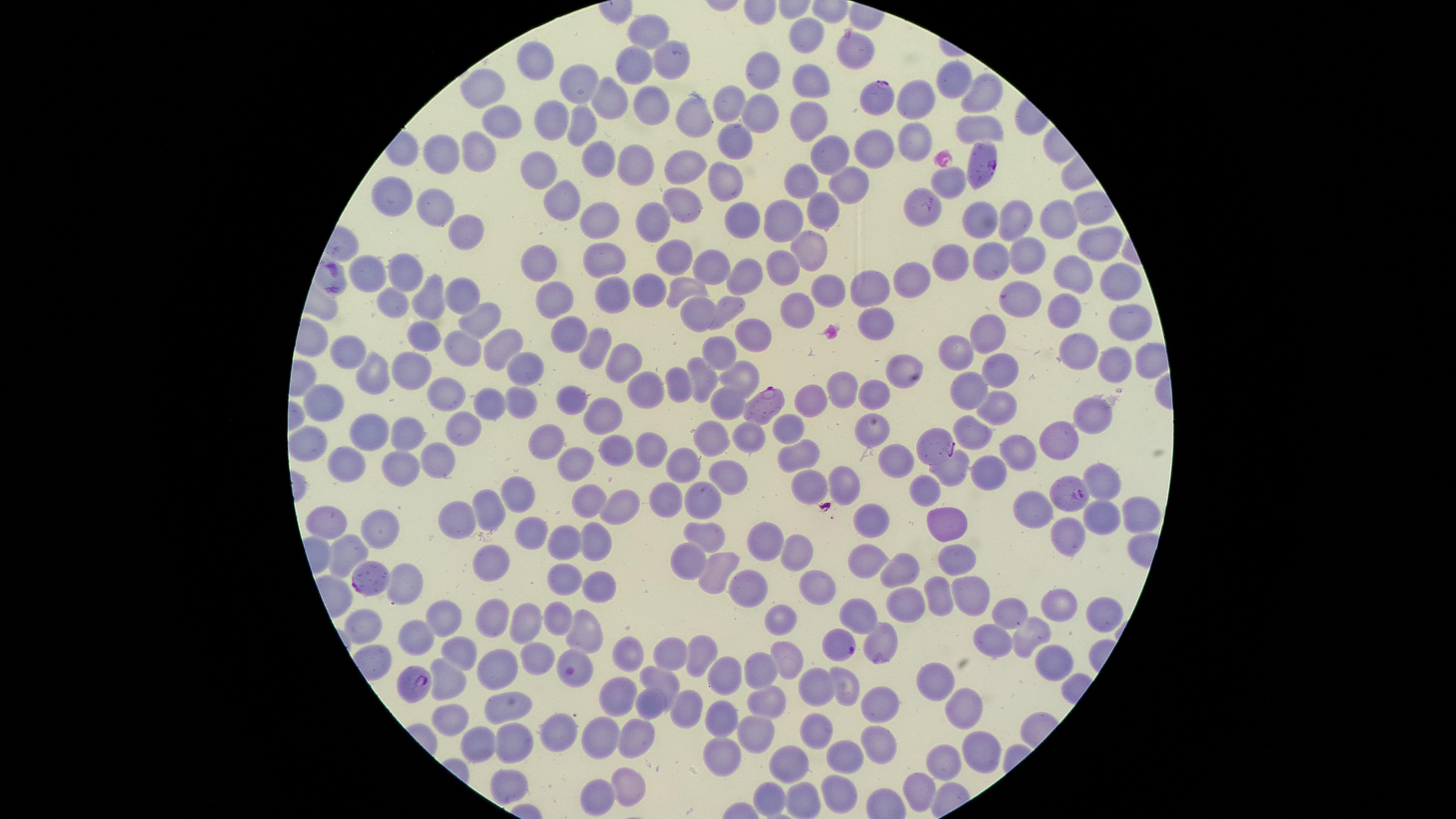

Approximate marker points as [x, y] in pixels.
Summary:
  - Parasitized red blood cells: [875, 93], [982, 163], [762, 403], [937, 445], [1065, 495], [373, 581], [838, 645], [877, 657], [573, 667], [417, 680]
  - Uninfected red blood cells: [806, 34], [649, 39], [861, 51], [537, 63], [662, 63], [633, 64], [768, 70], [810, 75], [957, 81], [588, 86], [489, 89], [980, 92], [609, 98], [916, 100], [724, 103], [762, 103], [656, 107], [690, 116], [503, 120], [551, 121], [804, 121], [580, 126], [976, 131], [913, 139], [732, 141], [480, 148], [876, 150], [830, 155], [446, 157], [597, 157], [642, 167], [686, 168], [540, 172], [851, 181], [951, 181], [805, 184], [724, 186], [396, 198], [433, 201], [558, 201], [681, 203], [916, 204], [823, 208], [597, 216], [1054, 216], [746, 217], [979, 219], [784, 220], [1012, 220], [652, 221], [465, 231], [1088, 244], [808, 248], [676, 255], [603, 257], [1024, 258], [550, 259], [991, 260], [712, 261], [949, 265], [411, 266], [786, 266], [372, 270], [1066, 272], [913, 277], [1108, 277], [747, 280], [833, 287], [456, 288], [649, 288], [688, 288], [866, 288], [602, 294], [551, 296], [1012, 297], [428, 304], [392, 305], [729, 306], [697, 308], [800, 310], [1061, 312], [476, 318], [876, 322], [1126, 323], [754, 331], [568, 333], [992, 335], [420, 343], [500, 348], [351, 349], [962, 349], [455, 350], [723, 351], [1074, 352], [594, 353], [620, 363], [1115, 365], [528, 367], [903, 367], [378, 370], [1003, 370], [409, 376], [703, 378], [743, 378], [844, 385], [680, 386], [649, 392], [965, 393], [869, 397], [450, 400], [573, 400], [810, 400], [493, 401], [526, 402], [326, 406], [727, 406], [1004, 409], [1096, 415], [612, 416], [789, 425], [453, 431], [978, 431], [873, 433], [367, 435], [406, 436], [716, 436], [748, 436], [550, 439], [1058, 439], [314, 445], [655, 449], [622, 450], [441, 456], [797, 456], [1022, 456], [891, 461], [399, 462], [678, 462], [580, 464], [345, 465], [960, 468], [994, 472], [731, 473], [1096, 480], [848, 483], [806, 487], [931, 488], [515, 493], [706, 498], [592, 499], [665, 500], [617, 506], [491, 507], [1041, 508], [1135, 511], [337, 514], [870, 516], [1099, 516], [384, 519], [460, 522], [952, 523], [532, 531], [707, 535], [1065, 537], [569, 538], [598, 541], [764, 541], [348, 549], [797, 550], [960, 553], [485, 556], [689, 561], [869, 561], [902, 568], [715, 573], [405, 580], [568, 580], [819, 584], [602, 587], [752, 588], [970, 589], [938, 590], [905, 602], [1064, 602], [1013, 612], [562, 613], [522, 616], [1099, 616], [493, 617], [782, 617], [859, 617], [446, 619], [370, 627], [588, 631], [1032, 631], [419, 632], [991, 636], [629, 646], [699, 650], [670, 651], [461, 652], [786, 654], [540, 657], [1051, 663], [763, 666], [730, 669], [505, 670], [661, 680], [450, 683], [938, 683], [851, 688], [810, 691], [617, 692], [765, 699], [506, 703], [963, 704], [651, 706], [884, 710], [727, 711], [686, 712], [451, 726], [754, 731], [604, 734], [560, 735], [811, 735], [631, 736], [512, 738], [481, 743], [882, 747], [722, 753], [851, 756], [979, 756], [789, 761], [942, 761], [621, 783], [508, 785], [841, 790], [923, 790], [593, 796], [765, 799], [801, 803]
  - Stain: Giemsa
  - Species: Plasmodium falciparum
  - Presence: malaria parasites detected
  - Preparation: thin blood smear
  - Field of view: single
  - Visible region: circular
  - Capture: smartphone photograph through the microscope eyepiece
  - Image size: 1456×819 pixels